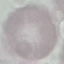

Summary:
  - Malaria status: uninfected
  - Preparation: thin blood smear
  - Stain: Giemsa
  - Image type: automatically extracted cell patch, resized to 64 × 64 pixels
  - Capture: smartphone camera at the microscope eyepiece